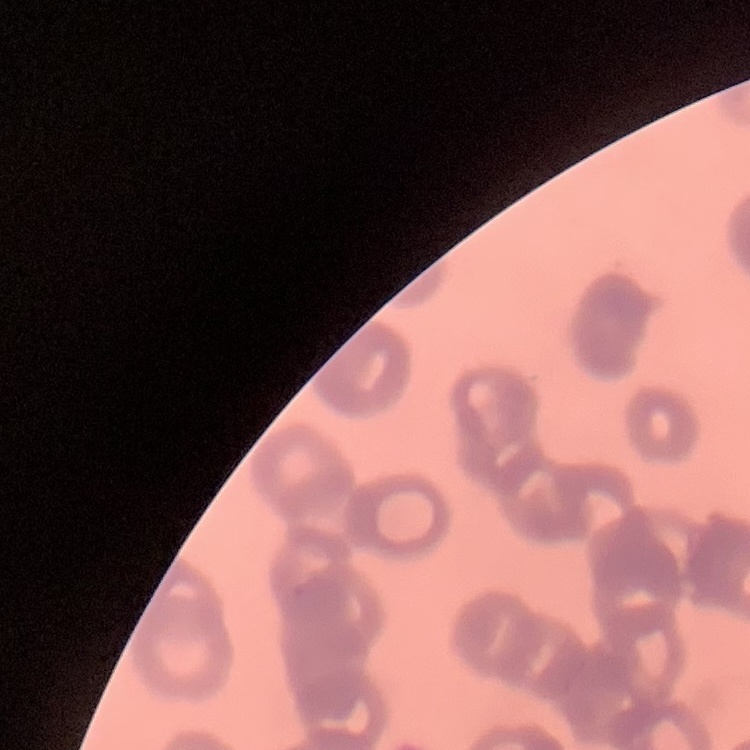

Summary:
  - Red blood cell morphology: rouleaux formation
  - Image type: square crop of a larger photomicrograph
  - Stain: Field's or Giemsa
  - Preparation: thin blood film